Locate every Plasmodium vivax-infected red blood cell.
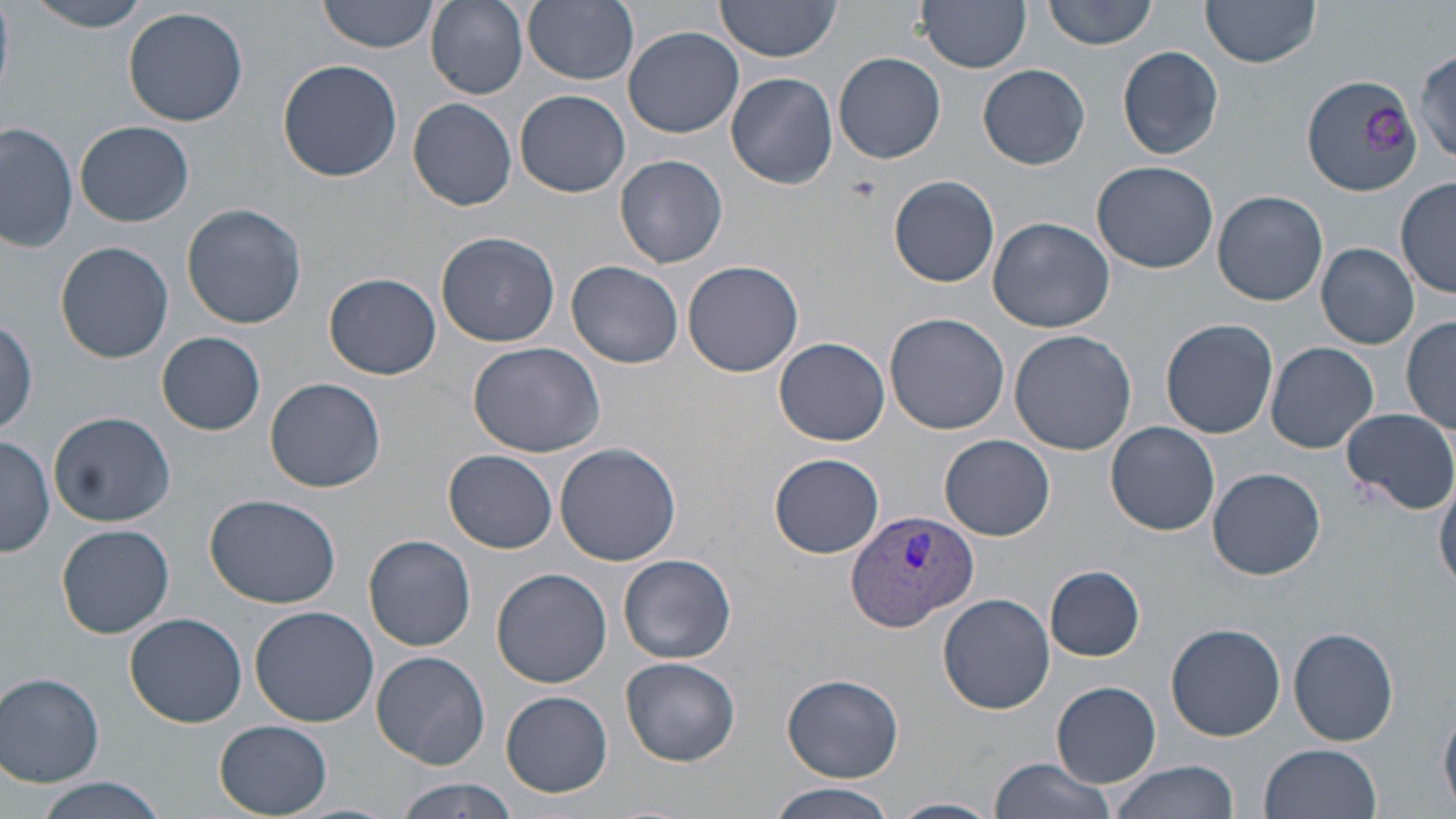
Approximate bounding boxes as (x1,y1)-(x2,y2) corner pairs in pixels.
Plasmodium vivax-infected red blood cells: (844,508)-(979,634).

Uninfected red blood cell locations: (27,0)-(155,31), (318,0)-(438,54), (427,0)-(529,100), (523,0)-(641,84), (715,0)-(843,60), (918,0)-(1031,72), (1043,0)-(1159,50), (1201,0)-(1322,68), (123,7)-(249,127), (622,27)-(746,138), (1117,46)-(1224,162), (1412,47)-(1456,163), (833,52)-(947,164), (276,57)-(402,181), (979,65)-(1090,169), (725,72)-(839,188), (1303,77)-(1420,200), (515,89)-(630,198), (408,98)-(517,210), (0,121)-(78,252), (77,121)-(196,227), (615,154)-(728,268), (1093,161)-(1218,273), (890,176)-(1000,287), (1398,177)-(1454,300), (1213,190)-(1328,306), (183,204)-(307,329), (986,216)-(1115,333), (436,230)-(560,347), (57,241)-(174,363), (1316,243)-(1420,349), (567,259)-(684,369), (682,260)-(804,377), (325,273)-(441,379), (884,313)-(1010,435), (0,314)-(40,440), (1402,316)-(1456,436), (1161,318)-(1278,439), (1009,329)-(1136,456), (159,332)-(266,434), (775,337)-(890,446), (468,341)-(605,458), (1265,341)-(1379,453), (265,377)-(385,493), (1340,407)-(1456,513), (49,411)-(176,527), (1105,420)-(1220,536), (940,435)-(1055,540), (1,436)-(54,558), (554,443)-(682,567), (444,449)-(558,553), (769,453)-(885,559), (1207,467)-(1326,580), (1434,473)-(1456,591), (205,494)-(343,608), (57,524)-(174,638), (365,535)-(477,651), (619,553)-(736,664), (1045,566)-(1145,661), (492,567)-(612,688), (938,593)-(1055,716), (250,605)-(380,726), (124,613)-(248,728), (1166,623)-(1286,741), (1289,627)-(1399,747), (371,651)-(490,768), (621,657)-(741,763), (782,672)-(903,782), (0,673)-(107,787), (1052,683)-(1161,787), (501,692)-(612,796), (215,720)-(333,816), (1258,743)-(1382,819), (986,756)-(1117,819), (1108,759)-(1240,819), (29,777)-(170,819), (391,779)-(521,818), (769,784)-(898,819), (889,796)-(1001,819). Slide-level diagnosis: Plasmodium vivax. Thin blood film. Image is 1456×819 pixels. Optical microscopy. May-Grünwald-Giemsa-stained preparation. Captured at 1000x magnification. One field of a larger specimen.